State the blood parasite species.
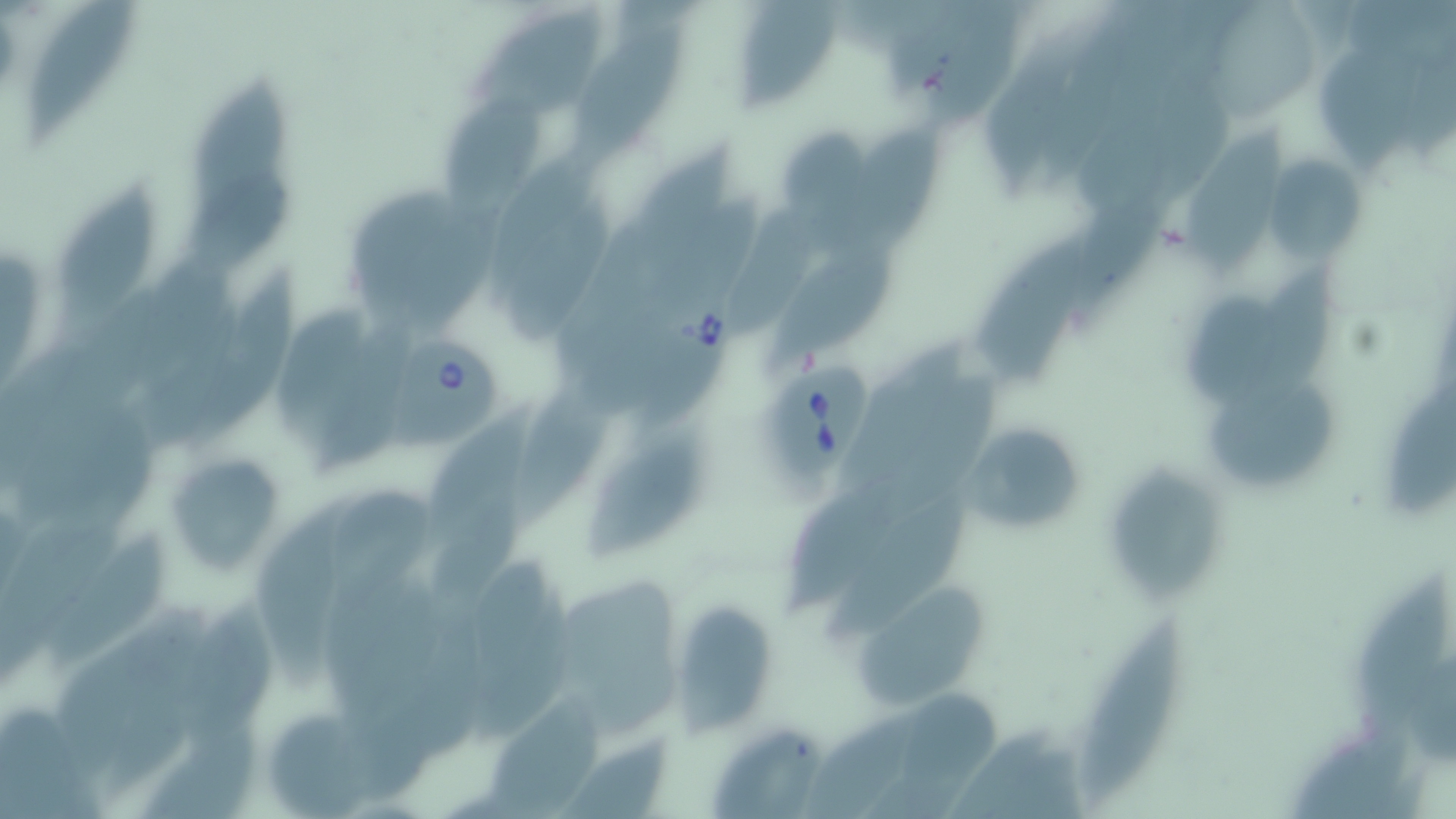

Babesia divergens.

Summary:
  - Coordinate format: approximate bounding boxes as (x1,y1)-(x2,y2) corner pairs in pixels
  - Uninfected red blood cell locations: (22,0)-(137,151), (736,1)-(843,115), (927,2)-(1028,138), (470,6)-(610,119), (570,20)-(698,168), (981,29)-(1097,197), (1323,50)-(1427,192), (192,75)-(296,233), (442,85)-(555,230), (776,125)-(872,224), (1179,126)-(1291,277), (817,127)-(950,257), (1265,153)-(1368,264), (56,176)-(166,335), (1063,185)-(1174,314), (508,201)-(610,342), (971,237)-(1087,389), (769,240)-(903,374), (1249,259)-(1344,389), (200,265)-(306,445), (1188,289)-(1290,409), (313,325)-(418,476), (845,340)-(965,491), (515,374)-(619,532), (1383,375)-(1456,522), (1210,379)-(1338,491), (419,394)-(555,549), (959,419)-(1089,538), (587,438)-(708,556), (164,454)-(287,574), (1105,463)-(1219,612), (788,472)-(937,617), (247,483)-(359,694), (826,499)-(966,643), (44,530)-(168,675), (1356,576)-(1451,736), (856,584)-(989,707), (181,599)-(279,755), (671,602)-(778,734), (1076,616)-(1182,805), (872,686)-(1017,819), (484,696)-(606,819), (798,708)-(923,819), (710,726)-(823,818), (555,736)-(673,819)
  - Babesia divergens-infected red blood cell locations: (632,279)-(746,439), (385,332)-(502,459), (766,354)-(873,490)
  - Preparation: thin blood smear
  - Modality: light microscopy
  - Stain: May-Grünwald-Giemsa
  - Field of view: one of a larger specimen
  - Magnification: 1000x
  - Image size: 1456×819 pixels